Assess the morphology of the erythrocytes.
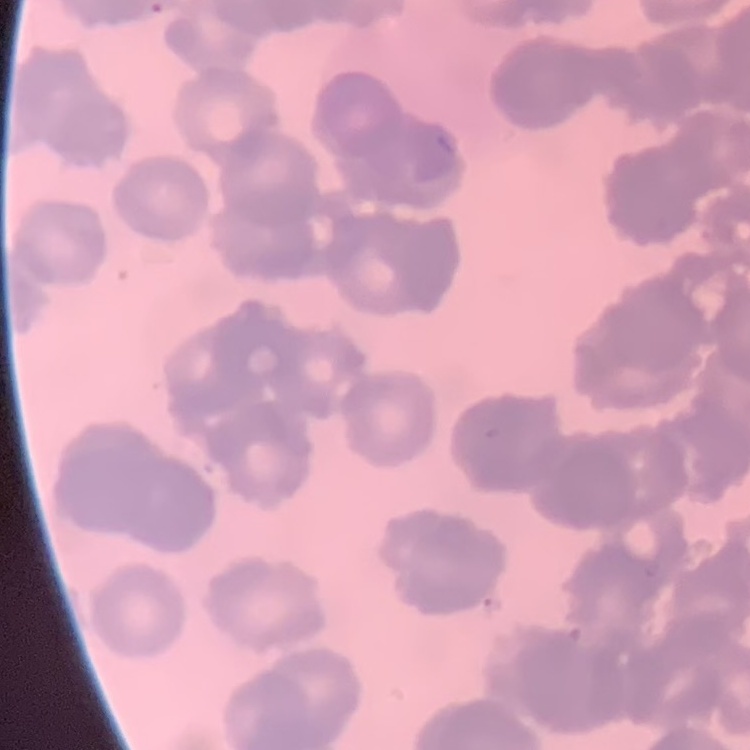

They show rouleaux formation.

stain = Field's or Giemsa
preparation = thin peripheral smear
image type = one tile cut from a larger photomicrograph